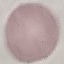
{
  "malaria_status": "uninfected",
  "preparation": "thin smear",
  "stain": "Giemsa",
  "capture": "smartphone camera at the microscope eyepiece",
  "image_type": "automatically extracted cell patch, resized to 64 × 64 pixels"
}